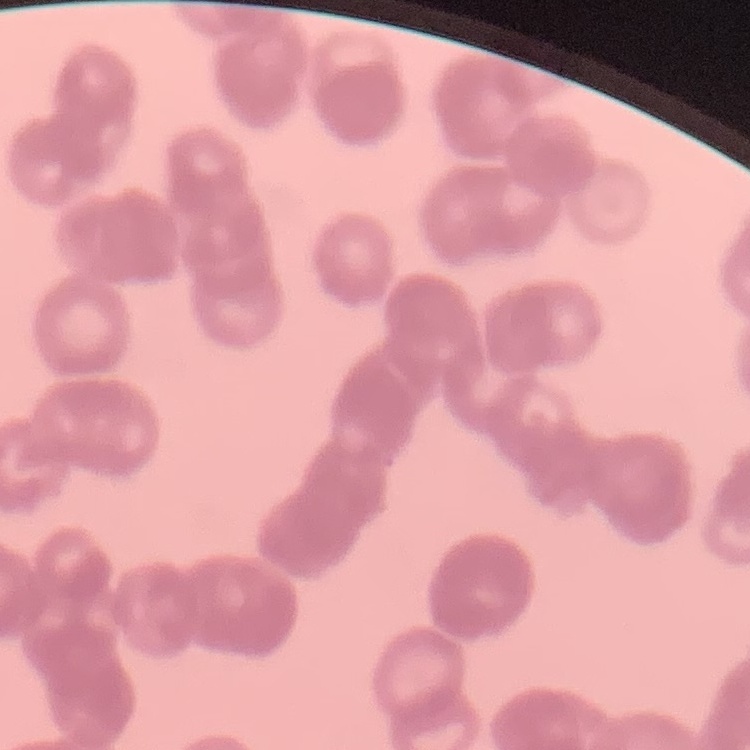 The erythrocytes exhibit rouleaux formation. Square crop of a larger photomicrograph. Field's or Giemsa stain. Thin blood smear.